State the blood parasite species.
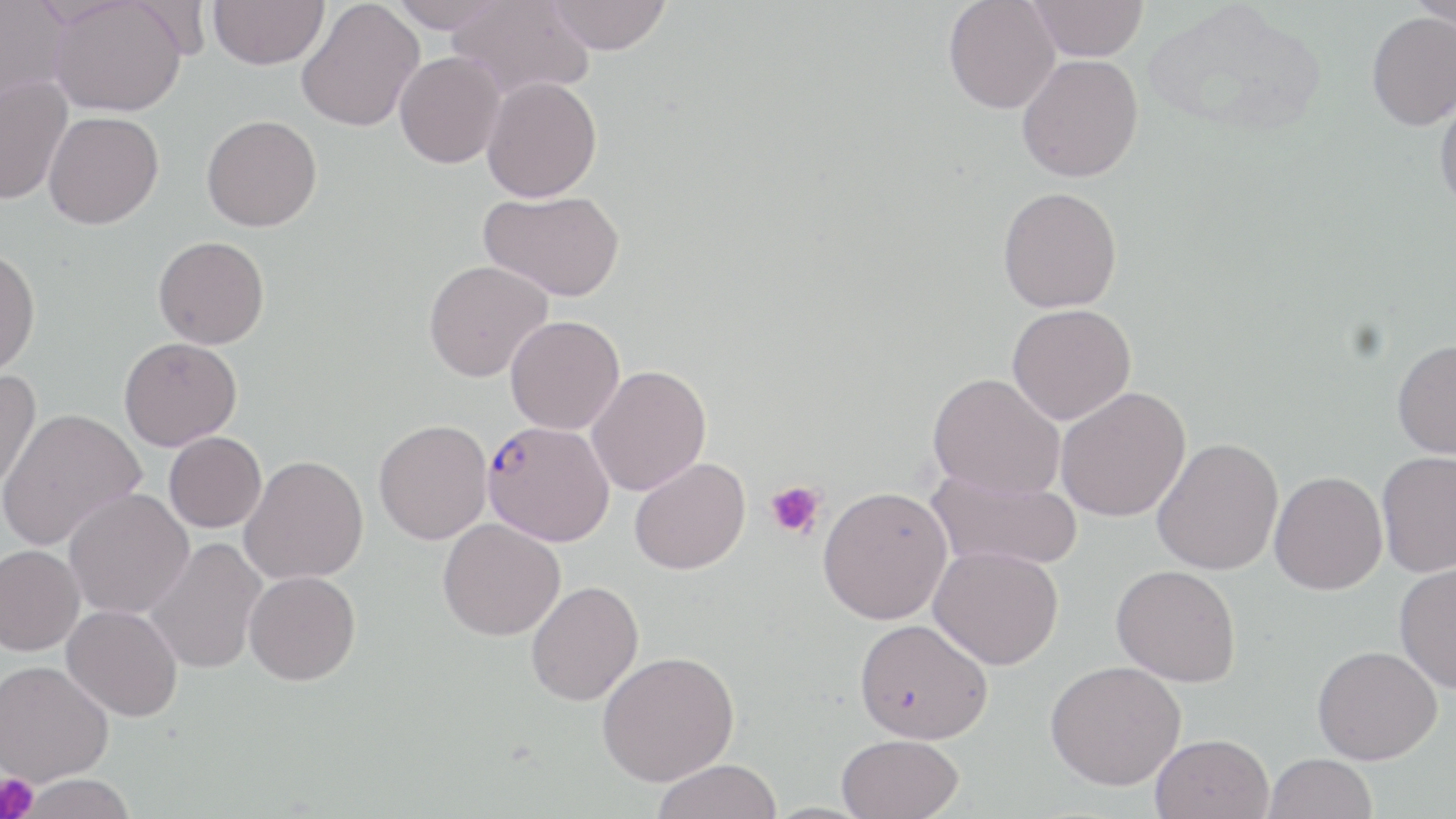
Plasmodium falciparum.

field of view = one of a larger specimen
magnification = 1000x
modality = light microscopy
stain = May-Grünwald-Giemsa
Plasmodium falciparum-infected red blood cell locations = approximate bounding boxes as named x1/y1/x2/y2 corners in pixels: (x1=483, y1=426, x2=617, y2=552)
preparation = thin blood film
platelet locations = approximate bounding boxes as named x1/y1/x2/y2 corners in pixels: (x1=765, y1=479, x2=825, y2=540), (x1=0, y1=773, x2=38, y2=819)
uninfected red blood cell locations = approximate bounding boxes as named x1/y1/x2/y2 corners in pixels: (x1=0, y1=0, x2=71, y2=104), (x1=50, y1=0, x2=187, y2=117), (x1=209, y1=0, x2=329, y2=70), (x1=386, y1=0, x2=510, y2=32), (x1=448, y1=0, x2=595, y2=102), (x1=547, y1=0, x2=672, y2=54), (x1=943, y1=0, x2=1060, y2=114), (x1=1143, y1=0, x2=1328, y2=139), (x1=1407, y1=0, x2=1456, y2=33), (x1=296, y1=1, x2=424, y2=132), (x1=1029, y1=1, x2=1149, y2=61), (x1=1366, y1=11, x2=1456, y2=131), (x1=394, y1=52, x2=505, y2=169), (x1=1017, y1=54, x2=1144, y2=182), (x1=481, y1=75, x2=602, y2=202), (x1=0, y1=76, x2=72, y2=206), (x1=1433, y1=89, x2=1456, y2=214), (x1=43, y1=111, x2=164, y2=229), (x1=201, y1=114, x2=322, y2=231), (x1=997, y1=186, x2=1122, y2=313), (x1=479, y1=189, x2=625, y2=301), (x1=153, y1=235, x2=269, y2=349), (x1=0, y1=248, x2=41, y2=379), (x1=423, y1=260, x2=553, y2=382), (x1=1007, y1=304, x2=1136, y2=425), (x1=505, y1=315, x2=625, y2=435), (x1=119, y1=336, x2=242, y2=450), (x1=1391, y1=339, x2=1456, y2=459), (x1=586, y1=364, x2=712, y2=496), (x1=0, y1=368, x2=42, y2=493), (x1=928, y1=372, x2=1066, y2=500), (x1=1055, y1=387, x2=1191, y2=522), (x1=0, y1=408, x2=146, y2=551), (x1=373, y1=419, x2=493, y2=545), (x1=163, y1=432, x2=267, y2=532), (x1=1152, y1=437, x2=1283, y2=576), (x1=1376, y1=451, x2=1456, y2=578), (x1=240, y1=454, x2=368, y2=585), (x1=629, y1=457, x2=751, y2=575), (x1=928, y1=468, x2=1083, y2=571), (x1=1269, y1=471, x2=1387, y2=595), (x1=818, y1=486, x2=952, y2=624), (x1=64, y1=488, x2=194, y2=619), (x1=438, y1=518, x2=565, y2=641), (x1=144, y1=537, x2=268, y2=675), (x1=0, y1=544, x2=84, y2=656), (x1=929, y1=545, x2=1064, y2=670), (x1=1394, y1=563, x2=1456, y2=694), (x1=1111, y1=565, x2=1241, y2=686), (x1=244, y1=570, x2=361, y2=685), (x1=526, y1=580, x2=644, y2=706), (x1=62, y1=604, x2=183, y2=722), (x1=854, y1=618, x2=993, y2=743), (x1=1312, y1=645, x2=1442, y2=765), (x1=597, y1=650, x2=739, y2=786), (x1=1045, y1=659, x2=1186, y2=791), (x1=0, y1=660, x2=114, y2=786), (x1=837, y1=733, x2=965, y2=819), (x1=1150, y1=733, x2=1274, y2=819), (x1=1264, y1=753, x2=1377, y2=819), (x1=651, y1=758, x2=783, y2=819), (x1=15, y1=774, x2=137, y2=819)
image size = 1456×819 pixels